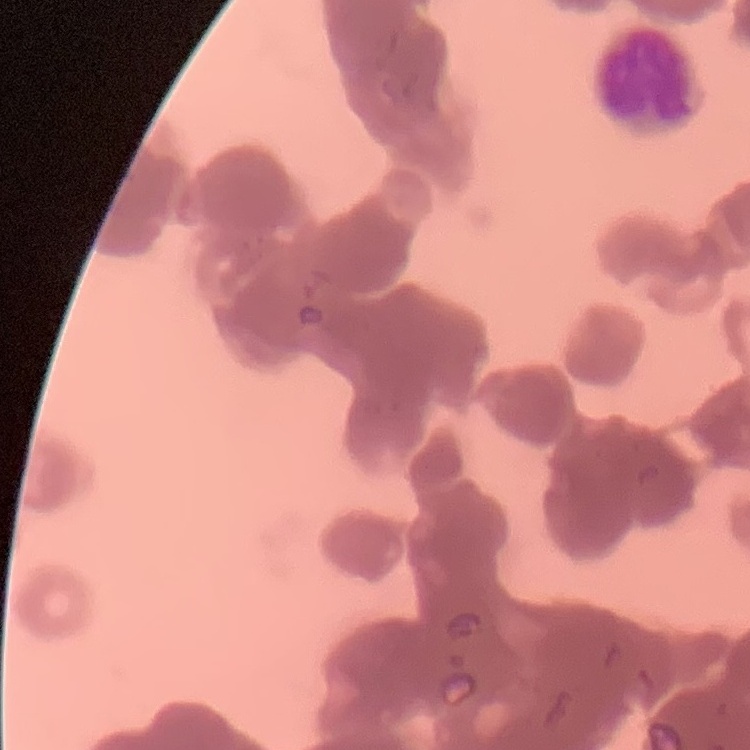
red blood cell morphology = rouleaux formation
image type = one tile cut from a larger photomicrograph
stain = Field's or Giemsa
preparation = thin peripheral smear